Locate and identify every blood parasite.
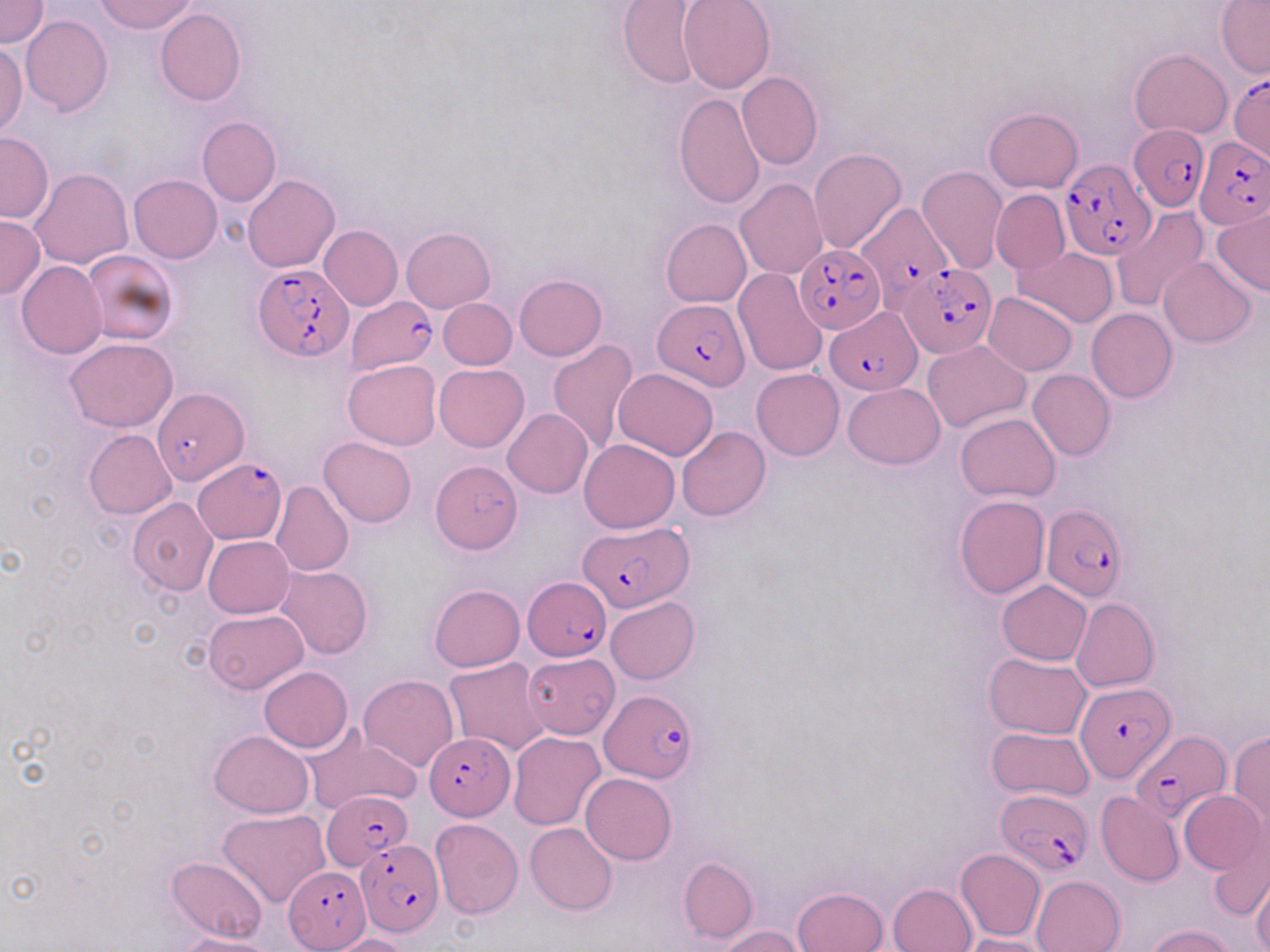
Approximate bounding boxes as (x1, y1, x2, y2) in pixels.
Plasmodium falciparum-infected red blood cells: (1229, 72, 1269, 165), (1129, 123, 1209, 211), (1196, 138, 1269, 227), (1060, 157, 1154, 261), (852, 198, 956, 309), (794, 245, 885, 334), (894, 258, 993, 355), (253, 262, 352, 361), (346, 294, 437, 373), (653, 299, 749, 389), (825, 307, 922, 394), (152, 390, 253, 489), (193, 457, 287, 544), (1041, 504, 1129, 603), (580, 521, 693, 611), (523, 577, 612, 662), (1076, 682, 1173, 782), (601, 690, 698, 785), (1132, 730, 1227, 821), (424, 733, 515, 818), (996, 788, 1092, 876), (321, 790, 412, 870), (355, 838, 442, 935), (282, 866, 371, 950).
No Plasmodium ovale, Plasmodium malariae, Plasmodium vivax, Babesia divergens, or Trypanosoma brucei observed.

Uninfected red blood cell locations: (0, 0, 48, 49), (95, 0, 200, 34), (678, 0, 774, 94), (1215, 0, 1269, 78), (617, 2, 708, 90), (155, 8, 246, 106), (21, 15, 113, 118), (0, 39, 27, 139), (1129, 49, 1234, 138), (738, 73, 823, 170), (673, 93, 766, 210), (983, 108, 1084, 194), (197, 116, 282, 206), (1, 132, 53, 224), (809, 147, 906, 254), (916, 166, 1007, 276), (31, 168, 133, 269), (128, 174, 222, 263), (243, 175, 339, 273), (734, 178, 828, 278), (990, 188, 1070, 276), (1110, 207, 1210, 313), (1212, 208, 1270, 297), (0, 215, 45, 302), (661, 218, 752, 307), (319, 225, 402, 310), (402, 226, 495, 312), (1013, 246, 1119, 327), (83, 248, 179, 346), (1158, 258, 1256, 347), (17, 262, 107, 359), (733, 269, 827, 376), (514, 273, 606, 360), (983, 292, 1077, 376), (438, 298, 517, 370), (934, 303, 1071, 404), (1085, 308, 1178, 402), (65, 338, 178, 433), (548, 340, 640, 458), (922, 341, 1029, 432), (343, 359, 441, 451), (433, 363, 529, 452), (613, 368, 719, 461), (752, 368, 844, 461), (1027, 369, 1116, 462), (843, 383, 944, 468), (503, 408, 592, 499), (956, 412, 1060, 501), (676, 426, 770, 521), (84, 430, 178, 519), (319, 437, 417, 527), (579, 439, 680, 533), (430, 458, 522, 555), (271, 479, 354, 576), (954, 495, 1050, 598), (127, 498, 219, 595), (202, 535, 295, 619), (276, 564, 373, 658), (996, 580, 1091, 665), (429, 585, 524, 673), (605, 596, 701, 684), (1071, 598, 1158, 693), (203, 609, 307, 693), (984, 652, 1091, 738), (523, 653, 619, 738), (444, 659, 554, 757), (258, 666, 353, 752), (359, 675, 457, 771), (301, 726, 422, 817), (987, 728, 1094, 801), (209, 730, 313, 817), (508, 731, 605, 830), (1228, 731, 1270, 830), (581, 773, 677, 864), (1179, 789, 1266, 875), (1096, 791, 1183, 886), (217, 809, 330, 908), (431, 818, 523, 919), (525, 822, 617, 914), (1208, 824, 1270, 922), (955, 847, 1046, 942), (168, 855, 268, 944), (678, 856, 757, 945), (1030, 875, 1125, 952), (1253, 875, 1270, 952), (889, 883, 976, 952), (793, 887, 888, 952), (1144, 924, 1234, 952), (716, 925, 806, 951), (177, 934, 281, 952), (330, 934, 413, 952), (959, 934, 1054, 952). Slide-level diagnosis: Plasmodium falciparum. Captured at 1000x magnification. One field of a larger specimen. Light microscopy. Image is 1270×952 pixels. Thin blood smear. May-Grünwald-Giemsa stain.